Comment on the morphology of the red blood cells.
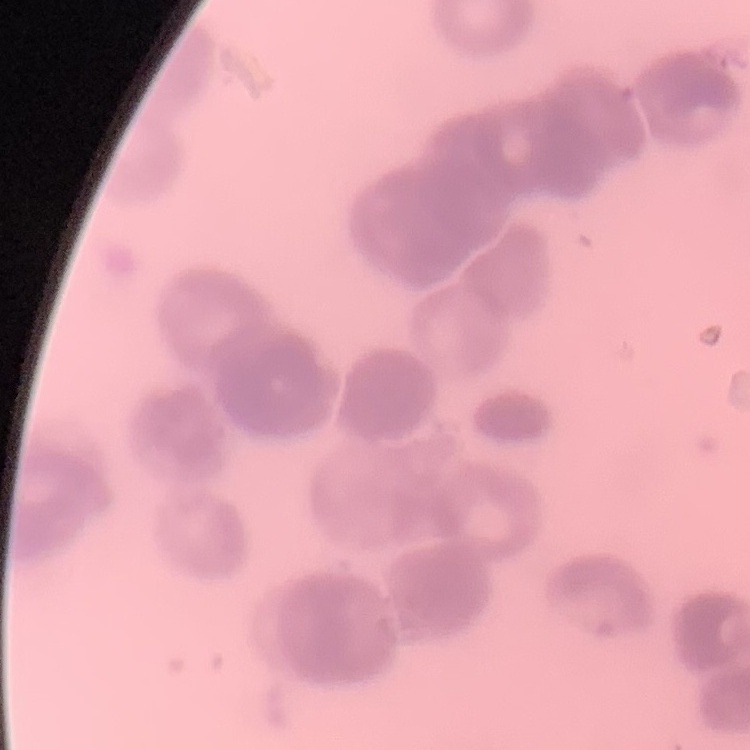
They show rouleaux formation.

stain = Field's or Giemsa
preparation = thin peripheral smear
image type = one tile cut from a larger photomicrograph